Identify the parasite.
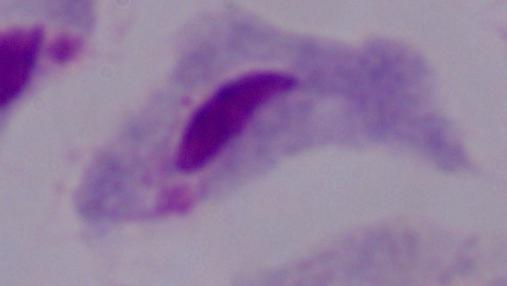

A trichomonad.

magnification = 1000x
modality = photomicrograph